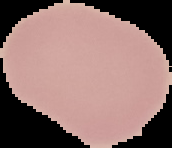

Summary:
  - Preparation: thin blood film
  - Image size: 172×148 pixels
  - Result: negative for Plasmodium parasites
  - Image type: segmented cell region on a black background